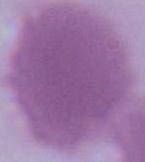

An erythrocyte is seen. Captured at 1000x magnification. Micrograph.